Assess this cell for malaria.
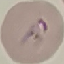

It is parasitized.

stain = Giemsa
capture = smartphone through the microscope eyepiece
image type = automatically extracted cell patch, resized to 64 × 64 pixels
preparation = thin smear